State which parasite is depicted.
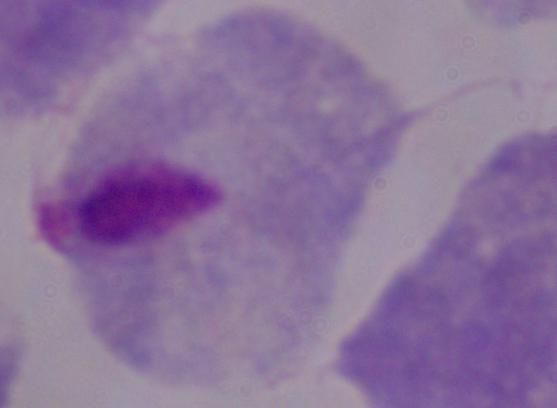
This is a trichomonad.

Summary:
  - Modality: photomicrograph
  - Magnification: 1000x